Comment on the morphology of the erythrocytes.
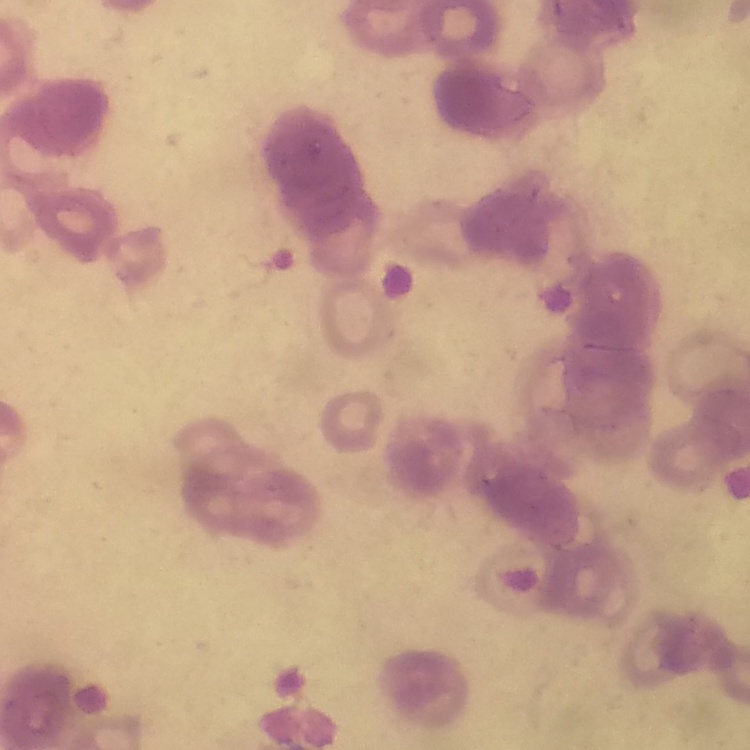

They show rouleaux formation.

image type = square crop of a larger photomicrograph
stain = Field's or Giemsa
preparation = thin peripheral smear